Comment on the morphology of the erythrocytes.
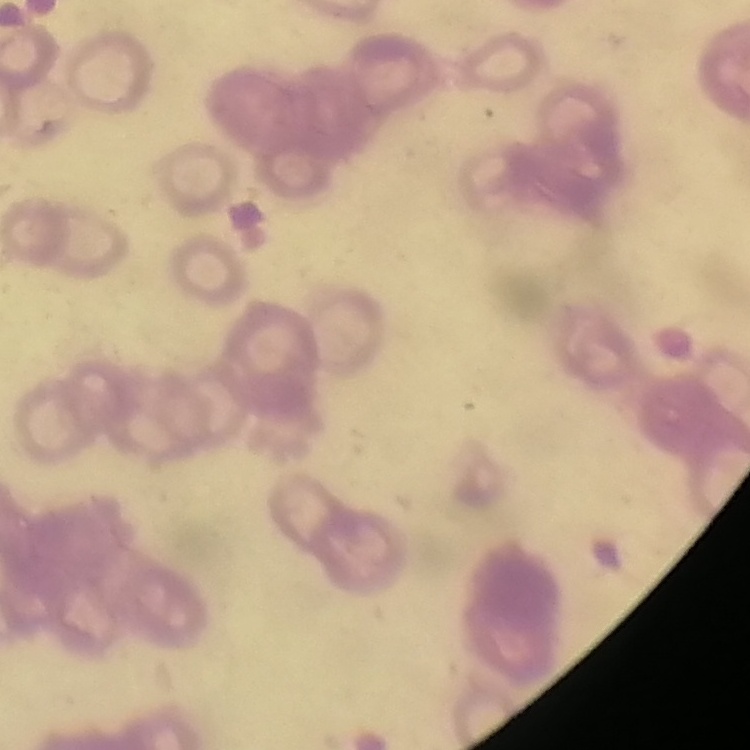
Rouleaux formation.

image type = square crop of a larger photomicrograph
preparation = thin blood film
stain = Field's or Giemsa